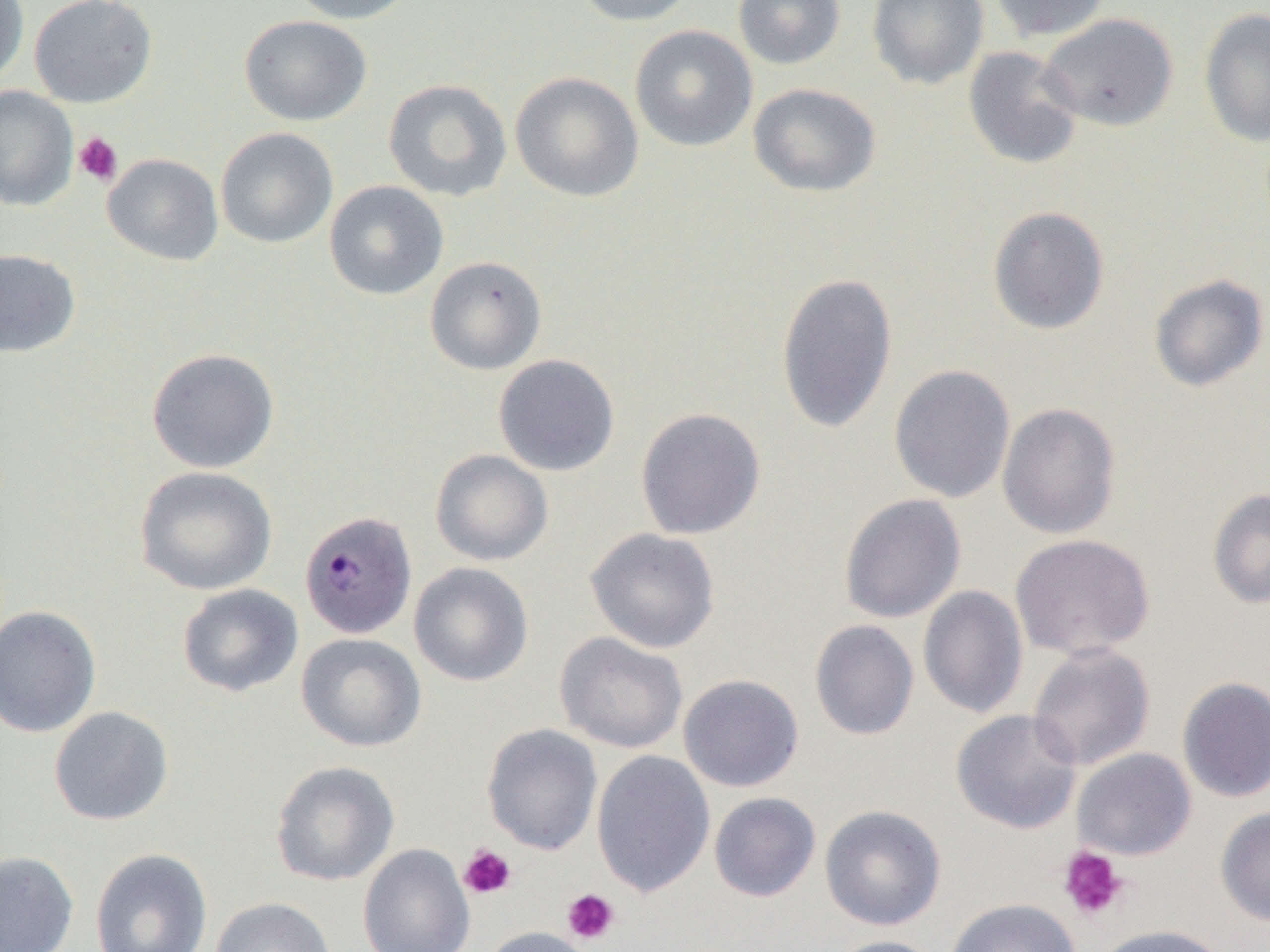

Approximate bounding boxes as (x1,y1)-(x2,y2) corner pairs in pixels. Platelet locations: (73,132)-(123,186), (458,844)-(517,900), (1058,846)-(1129,922), (562,889)-(620,944). Uninfected red blood cell locations (subset): (0,0)-(29,86), (29,0)-(157,108), (286,0)-(419,24), (572,0)-(699,26), (732,0)-(846,70), (866,0)-(990,90), (988,0)-(1112,42), (1198,8)-(1270,147), (1038,13)-(1178,131), (239,15)-(373,126), (630,25)-(758,152), (963,46)-(1083,170), (510,71)-(644,202), (383,79)-(512,202), (747,83)-(881,198), (0,85)-(79,211), (215,127)-(338,248), (102,153)-(224,266), (324,180)-(449,300), (987,206)-(1111,336), (0,248)-(81,358), (425,255)-(547,375), (775,272)-(899,434), (1149,273)-(1269,392), (146,347)-(279,474), (493,354)-(621,476), (888,364)-(1016,504), (997,402)-(1121,540), (635,407)-(766,540), (430,449)-(553,567), (134,466)-(278,596), (1207,488)-(1270,609), (839,493)-(966,623), (585,527)-(721,654), (1010,533)-(1155,660), (409,562)-(534,686), (177,583)-(304,697), (918,585)-(1029,719), (0,605)-(102,738), (810,619)-(919,740), (554,631)-(688,754), (296,632)-(427,752), (1027,643)-(1155,771), (678,674)-(804,792), (1177,676)-(1270,803), (48,706)-(173,826), (950,709)-(1083,835), (482,723)-(603,856), (1072,748)-(1196,861), (592,750)-(716,897), (270,760)-(401,886), (709,792)-(821,902), (819,804)-(947,931), (1216,807)-(1270,926), (357,843)-(475,952), (90,848)-(213,952), (0,851)-(79,952), (210,896)-(337,952), (944,898)-(1080,952), (1093,924)-(1229,952), (480,926)-(597,952), (825,935)-(946,952). Slide-level diagnosis: Plasmodium malariae. Thin blood smear. Optical microscopy. One field of a larger specimen. 1000x magnification. Image is 1270×952 pixels.